Locate and identify every blood parasite.
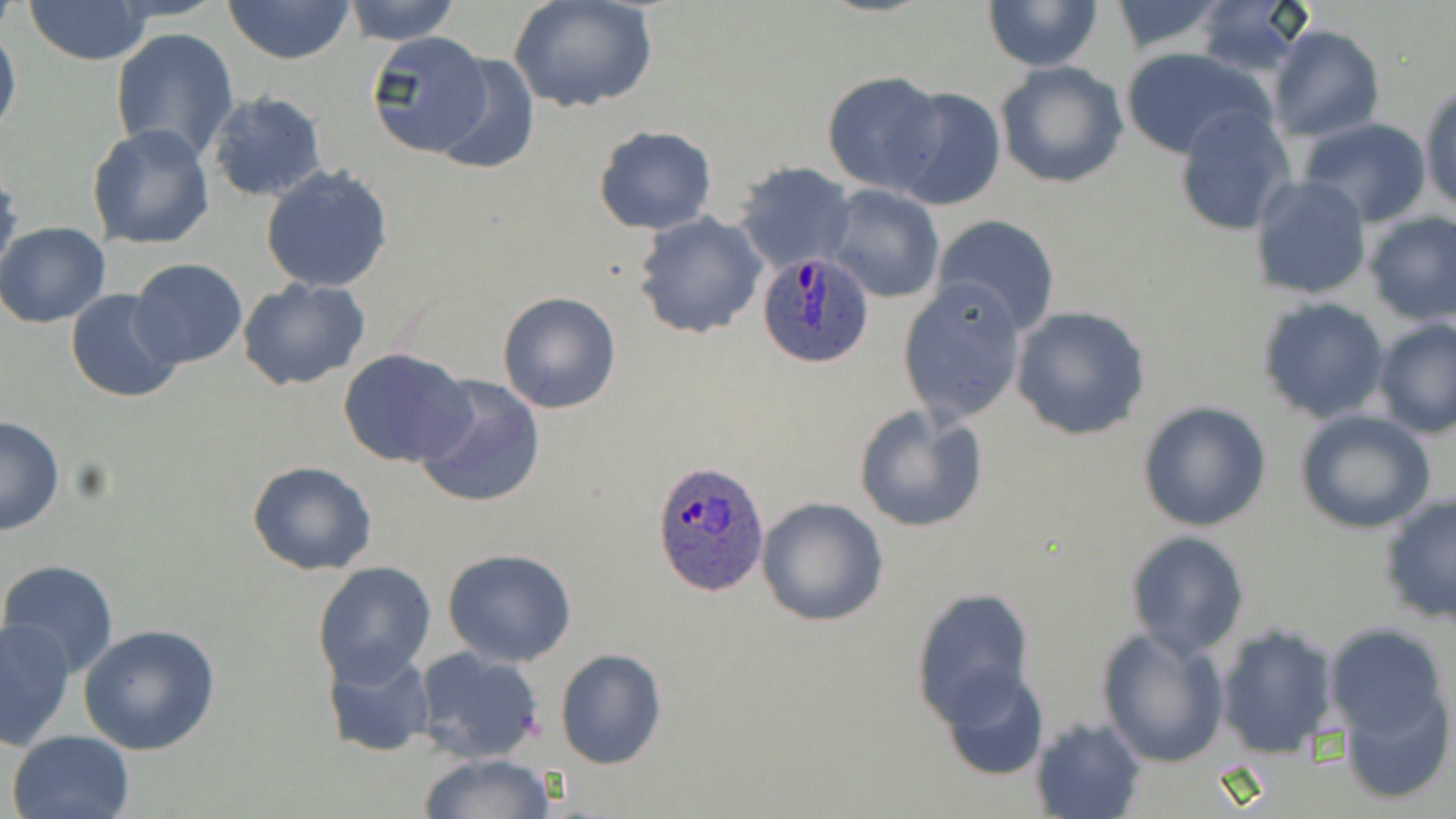
Approximate bounding boxes as [x1, y1, x2, y2] in pixels.
Plasmodium ovale-infected red blood cells: [756, 251, 873, 369], [653, 461, 769, 597].
No Plasmodium falciparum, Plasmodium malariae, Plasmodium vivax, Babesia divergens, or Trypanosoma brucei observed.

Uninfected red blood cell locations: [23, 0, 154, 66], [223, 0, 354, 64], [344, 0, 461, 43], [507, 0, 658, 115], [983, 1, 1104, 72], [1107, 1, 1230, 56], [1191, 1, 1316, 79], [0, 22, 21, 144], [1268, 25, 1385, 140], [109, 27, 239, 163], [364, 31, 494, 159], [1118, 46, 1275, 161], [430, 53, 538, 175], [994, 61, 1128, 189], [821, 71, 947, 196], [1419, 82, 1456, 215], [888, 87, 1005, 212], [205, 91, 328, 204], [1171, 105, 1297, 236], [1298, 118, 1432, 227], [86, 122, 216, 250], [594, 125, 717, 235], [736, 161, 855, 271], [0, 164, 19, 277], [260, 164, 393, 292], [1251, 175, 1371, 301], [824, 184, 945, 301], [634, 210, 768, 340], [1363, 211, 1456, 327], [931, 213, 1060, 336], [0, 221, 113, 328], [129, 259, 248, 369], [237, 277, 370, 390], [897, 279, 1029, 424], [66, 288, 183, 403], [497, 291, 621, 413], [1259, 298, 1391, 424], [1010, 306, 1152, 441], [1372, 319, 1456, 439], [338, 348, 475, 468], [413, 376, 547, 510], [1136, 401, 1273, 533], [853, 404, 989, 533], [1296, 410, 1437, 534], [0, 417, 65, 535], [247, 461, 377, 576], [1379, 494, 1455, 627], [756, 496, 889, 627], [1125, 530, 1250, 659], [442, 547, 577, 667], [1, 560, 118, 679], [312, 561, 436, 686], [910, 587, 1035, 727], [2, 618, 77, 750], [1324, 623, 1451, 741], [79, 624, 223, 757], [1215, 624, 1339, 759], [1094, 626, 1231, 768], [323, 645, 435, 757], [412, 647, 545, 764], [554, 647, 666, 770], [939, 667, 1050, 782], [1339, 688, 1453, 805], [1029, 715, 1146, 819], [6, 729, 135, 819], [418, 752, 557, 819]. Slide-level diagnosis: Plasmodium ovale. May-Grünwald-Giemsa-stained preparation. Thin blood film. 1000x magnification. Single field of view. Optical microscopy. Image is 1456×819 pixels.